Locate every malaria parasite.
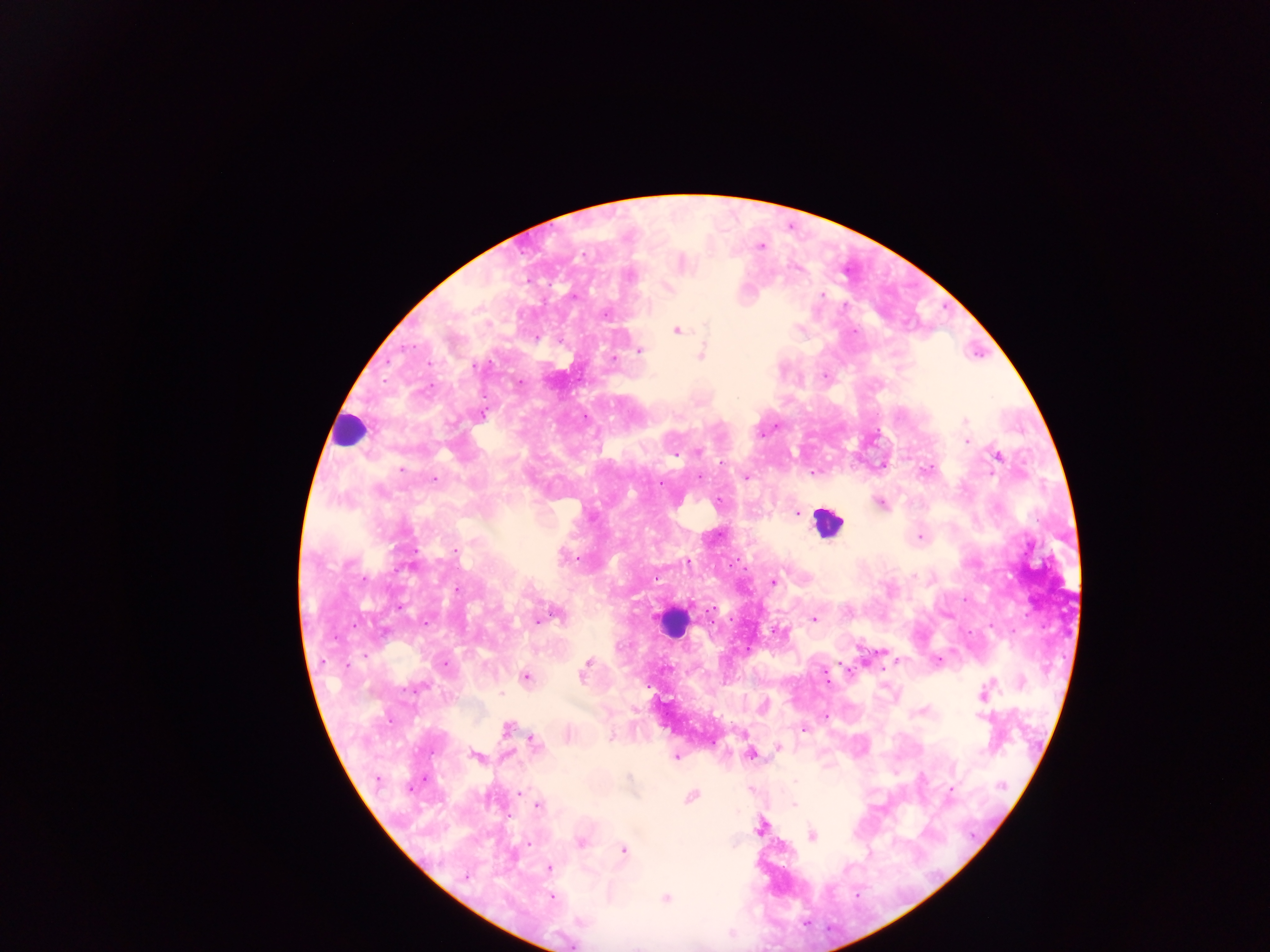

Approximate centers as {x, y} in pixels.
Malaria parasites: {760, 247}, {584, 256}, {629, 277}, {670, 288}, {823, 295}, {573, 296}, {605, 315}, {676, 331}, {535, 338}, {639, 350}, {701, 355}, {613, 358}, {475, 365}, {519, 382}, {482, 416}, {964, 421}, {966, 441}, {698, 452}, {675, 455}, {997, 456}, {722, 462}, {401, 470}, {812, 474}, {746, 477}, {435, 478}, {699, 478}, {660, 484}, {880, 503}, {797, 514}, {919, 537}, {455, 550}, {563, 557}, {573, 558}, {687, 561}, {773, 581}, {458, 590}, {401, 607}, {712, 609}, {558, 616}, {814, 619}, {538, 620}, {588, 662}, {444, 664}, {584, 672}, {825, 675}, {525, 677}, {414, 688}, {983, 694}, {980, 715}, {825, 716}, {507, 728}, {803, 730}, {611, 738}, {535, 742}, {778, 747}, {751, 754}, {475, 755}, {675, 756}, {377, 778}, {629, 778}, {796, 781}, {1002, 786}, {409, 789}, {950, 790}, {520, 794}, {691, 797}, {794, 804}, {537, 805}, {761, 827}, {812, 835}, {582, 842}, {528, 843}, {623, 850}, {549, 868}, {465, 877}, {552, 898}, {665, 898}, {580, 922}.

Leukocyte locations: {349, 429}, {828, 522}, {671, 621}. Thick blood film. Image is 1270×952 pixels. Mobile-phone photograph taken through the microscope. Collected in Ghana. Single field of view.